Report the malaria status.
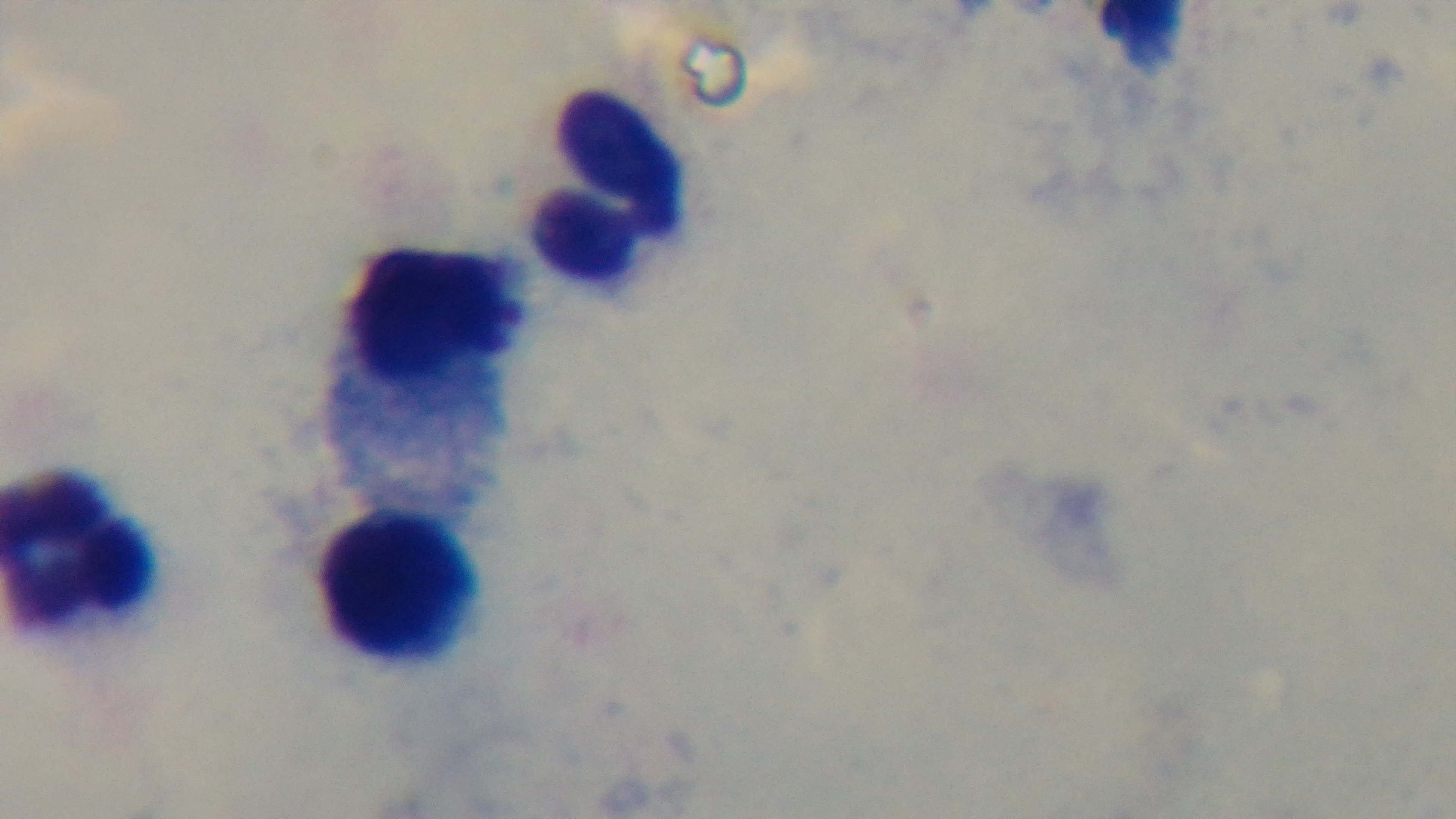
It is uninfected.

Summary:
  - Capture: mounted 4K digital camera
  - Objective: 100x oil immersion
  - Stain: Giemsa
  - Modality: light microscopy
  - Preparation: thick
  - Field of view: one from the slide